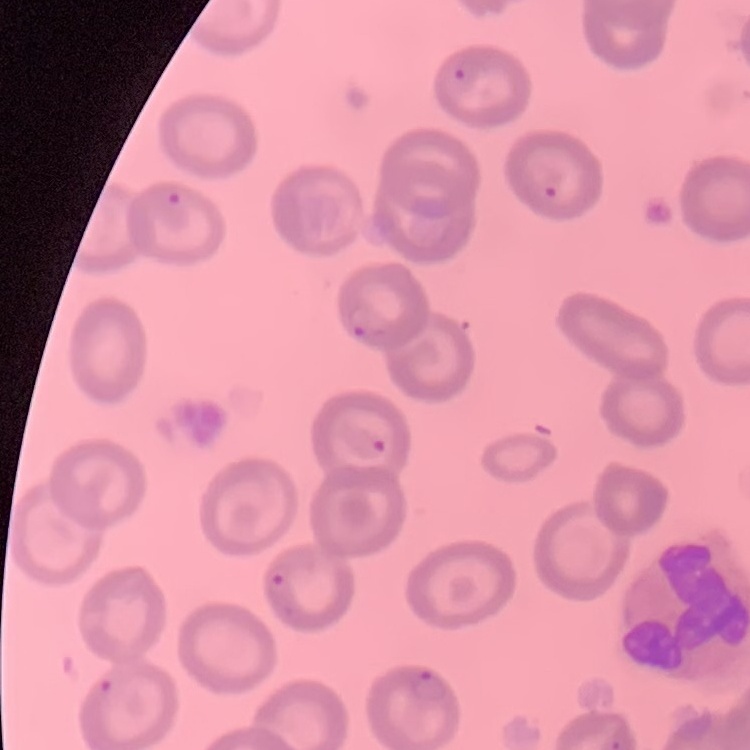

Summary:
  - Erythrocyte morphology: no rouleaux formation
  - Preparation: thin peripheral smear
  - Stain: Field's or Giemsa
  - Image type: one tile cut from a larger photomicrograph